Locate every uninfected red blood cell.
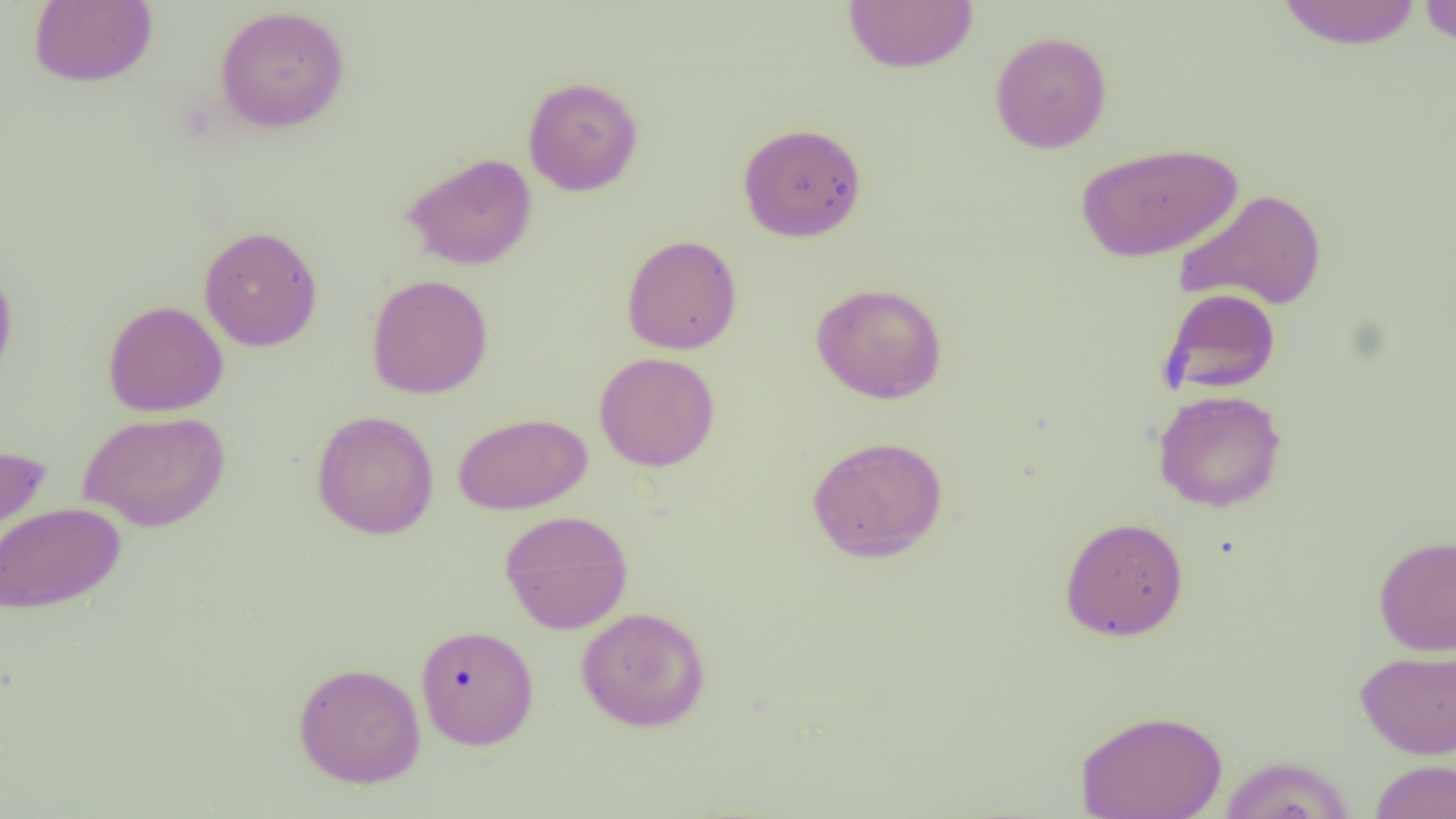
Approximate bounding boxes as (x1, y1, x2, y2) in pixels.
Uninfected red blood cells: (28, 0, 157, 88), (842, 1, 978, 73), (1276, 1, 1423, 49), (1418, 1, 1456, 46), (214, 5, 350, 134), (989, 31, 1112, 153), (522, 76, 644, 196), (738, 122, 867, 243), (1075, 141, 1244, 263), (402, 152, 537, 270), (1174, 187, 1328, 312), (199, 225, 322, 351), (621, 234, 742, 354), (0, 261, 18, 390), (366, 274, 493, 399), (810, 281, 948, 404), (1158, 288, 1282, 395), (102, 300, 228, 417), (594, 352, 720, 471), (1152, 389, 1287, 512), (311, 409, 439, 540), (78, 411, 230, 532), (453, 412, 592, 515), (806, 435, 949, 563), (0, 443, 50, 565), (0, 502, 125, 614), (499, 509, 633, 634), (1060, 516, 1189, 641), (1373, 534, 1456, 656), (576, 606, 711, 732), (415, 624, 539, 750), (1355, 647, 1456, 759), (293, 662, 426, 788), (1074, 708, 1228, 819), (1218, 755, 1355, 819), (1369, 759, 1456, 818).

Summary:
  - Slide-level diagnosis: negative for blood parasites
  - Preparation: thin blood smear
  - Modality: optical microscopy
  - Image size: 1456×819 pixels
  - Magnification: 1000x
  - Field of view: one of a larger specimen